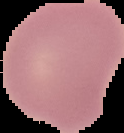
{
  "preparation": "thin blood film",
  "image_size": "124×133 pixels",
  "image_type": "segmented cell region on a black background",
  "result": "negative for malaria parasites"
}